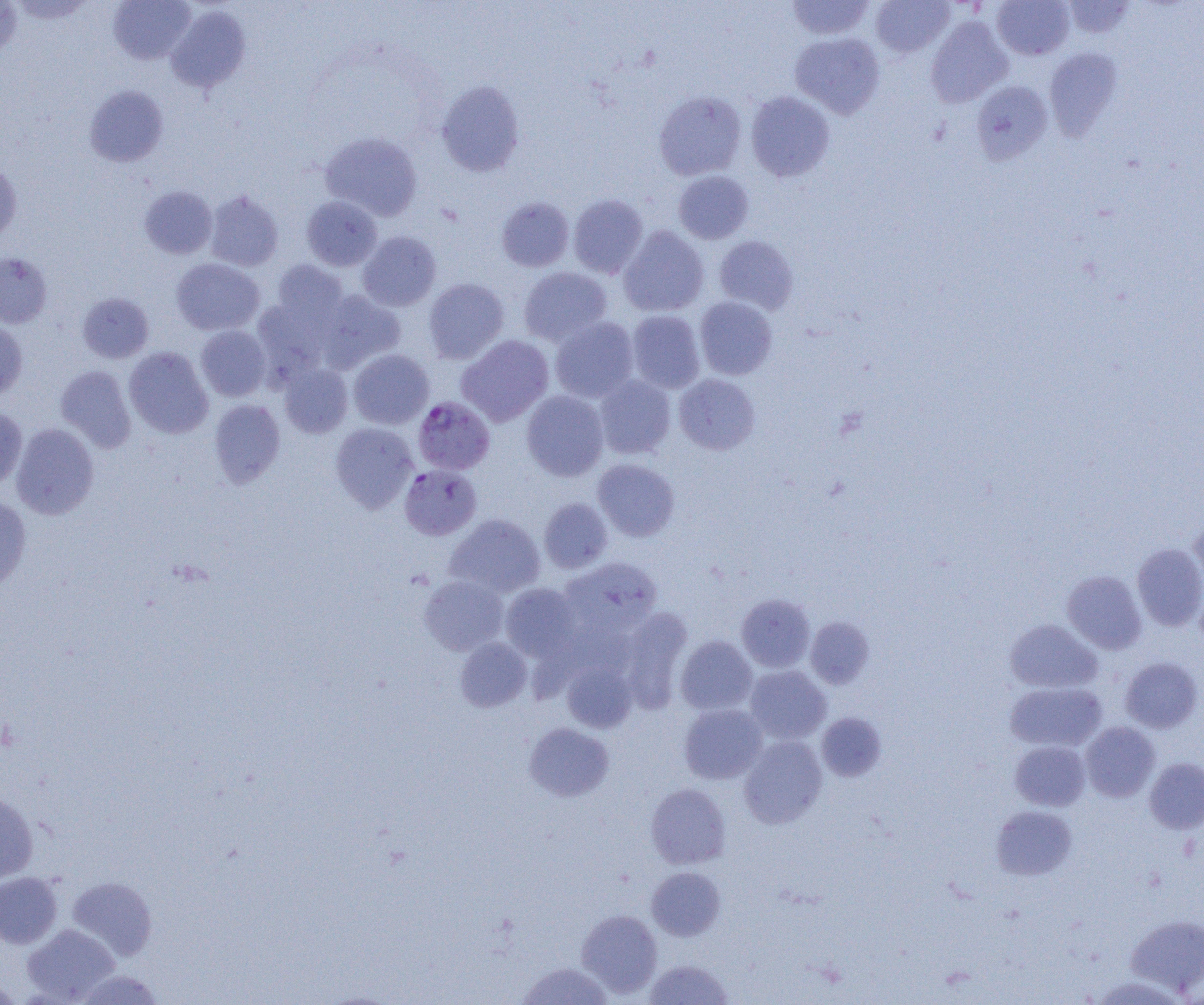

slide-level diagnosis = Plasmodium falciparum
uninfected red blood cell locations = approximate bounding boxes as (x1,y1)-(x2,y2) corner pairs in pixels: (9,0)-(96,24), (109,0)-(196,64), (786,0)-(874,40), (871,0)-(954,57), (991,0)-(1074,60), (1061,0)-(1138,40), (0,1)-(22,60), (166,5)-(251,92), (925,16)-(1013,108), (790,32)-(885,119), (1043,48)-(1123,140), (436,79)-(525,176), (971,80)-(1053,165), (84,85)-(168,167), (654,91)-(747,180), (746,91)-(835,182), (321,131)-(423,220), (0,160)-(22,243), (673,171)-(754,244), (138,185)-(217,259), (204,189)-(283,271), (568,194)-(648,278), (302,196)-(382,271), (496,197)-(574,272), (619,226)-(709,317), (357,231)-(441,311), (714,236)-(798,315), (0,252)-(52,328), (171,258)-(265,335), (271,260)-(348,328), (519,267)-(612,346), (424,278)-(509,364), (319,290)-(405,371), (78,292)-(154,363), (694,297)-(777,380), (627,310)-(705,392), (550,317)-(639,403), (0,319)-(28,400), (196,325)-(271,401), (457,335)-(554,427), (124,347)-(213,438), (348,350)-(434,429), (279,363)-(353,438), (55,366)-(136,452), (674,374)-(760,454), (594,376)-(675,459), (522,391)-(608,481), (210,398)-(285,488), (0,408)-(27,492), (10,422)-(99,519), (330,422)-(419,513), (592,458)-(680,541), (0,497)-(31,591), (539,498)-(613,573), (445,514)-(546,597), (1188,517)-(1204,598), (1132,543)-(1204,631), (560,556)-(663,635), (1061,570)-(1146,654), (419,575)-(508,655), (500,583)-(580,662), (736,593)-(815,672), (618,608)-(693,712), (805,616)-(874,689), (1004,619)-(1102,694), (676,636)-(757,715), (455,637)-(532,712), (1120,657)-(1203,732), (562,662)-(636,733), (745,665)-(831,744), (1005,682)-(1107,752), (679,704)-(767,784), (816,712)-(887,781), (524,722)-(614,802), (1081,722)-(1160,802), (739,735)-(827,828), (1010,740)-(1091,810), (1144,758)-(1204,834), (646,783)-(730,869), (0,790)-(39,884), (991,805)-(1076,880), (647,867)-(725,940), (0,872)-(62,948), (67,876)-(157,961), (577,909)-(662,998), (1126,915)-(1204,996), (21,923)-(120,1003), (645,959)-(733,1004), (517,961)-(614,1004), (0,977)-(24,1003)
image size = 1204×1005 pixels
modality = optical microscopy
Plasmodium falciparum-infected red blood cell locations = approximate bounding boxes as (x1,y1)-(x2,y2) corner pairs in pixels: (413,397)-(494,474), (399,464)-(482,540)
magnification = 1000x
preparation = thin blood smear
field of view = single